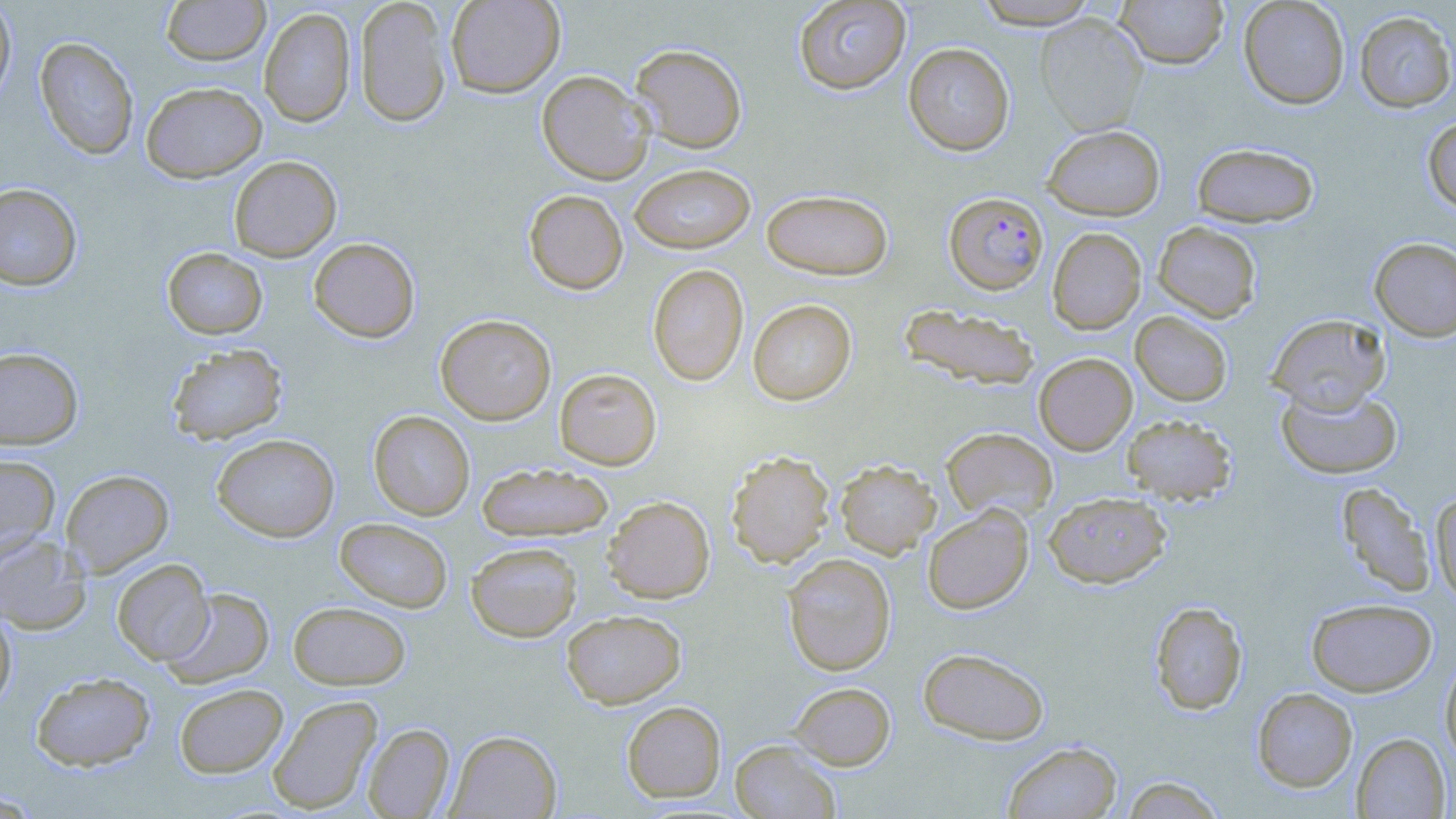
Summary:
  - Coordinate format: approximate bounding boxes as (x1, y1, x2, y2) in pixels
  - Plasmodium falciparum-infected red blood cell locations: (944, 192, 1049, 295)
  - Uninfected red blood cell locations: (160, 0, 270, 66), (354, 0, 452, 127), (445, 0, 565, 97), (793, 0, 911, 95), (1115, 0, 1229, 68), (1238, 0, 1350, 109), (0, 1, 16, 106), (973, 1, 1102, 29), (258, 7, 356, 127), (1354, 10, 1456, 113), (1035, 14, 1148, 136), (35, 37, 139, 159), (629, 43, 747, 153), (903, 43, 1015, 156), (537, 70, 654, 184), (141, 81, 267, 182), (1422, 115, 1456, 213), (1042, 125, 1165, 221), (1191, 142, 1320, 228), (228, 155, 342, 262), (629, 163, 756, 254), (0, 183, 83, 290), (761, 188, 894, 280), (523, 189, 628, 295), (1153, 221, 1262, 322), (1047, 227, 1146, 335), (308, 237, 420, 342), (1369, 237, 1456, 342), (163, 247, 267, 339), (647, 263, 749, 386), (747, 299, 857, 405), (898, 303, 1041, 391), (1130, 311, 1233, 406), (1266, 313, 1391, 412), (435, 314, 556, 425), (166, 343, 288, 445), (0, 346, 83, 450), (1033, 353, 1137, 455), (554, 368, 662, 470), (1276, 383, 1402, 479), (368, 410, 475, 520), (1121, 414, 1237, 504), (941, 427, 1058, 522), (212, 434, 339, 542), (725, 450, 835, 568), (0, 453, 60, 559), (835, 459, 941, 558), (477, 462, 614, 542), (61, 469, 173, 576), (1336, 481, 1435, 598), (1430, 490, 1456, 607), (1043, 491, 1172, 588), (602, 496, 715, 603), (922, 505, 1034, 615), (334, 518, 453, 612), (0, 534, 90, 634), (466, 541, 582, 641), (782, 552, 896, 676), (112, 559, 213, 665), (162, 587, 275, 688), (1306, 597, 1437, 696), (288, 601, 411, 690), (1149, 601, 1248, 715), (0, 606, 17, 714), (561, 609, 686, 708), (917, 647, 1050, 745), (1440, 656, 1456, 767), (32, 672, 155, 771), (789, 681, 895, 769), (173, 683, 288, 778), (1252, 687, 1358, 792), (267, 695, 382, 814), (621, 700, 726, 802), (363, 723, 455, 818), (446, 729, 562, 818), (1352, 732, 1451, 818), (730, 739, 841, 819), (1002, 741, 1122, 818), (1120, 774, 1227, 819), (0, 790, 44, 817)
  - Slide-level diagnosis: Plasmodium falciparum
  - Magnification: 1000x
  - Stain: May-Grünwald-Giemsa
  - Preparation: thin blood film
  - Modality: light microscopy
  - Image size: 1456×819 pixels
  - Field of view: one of a larger specimen